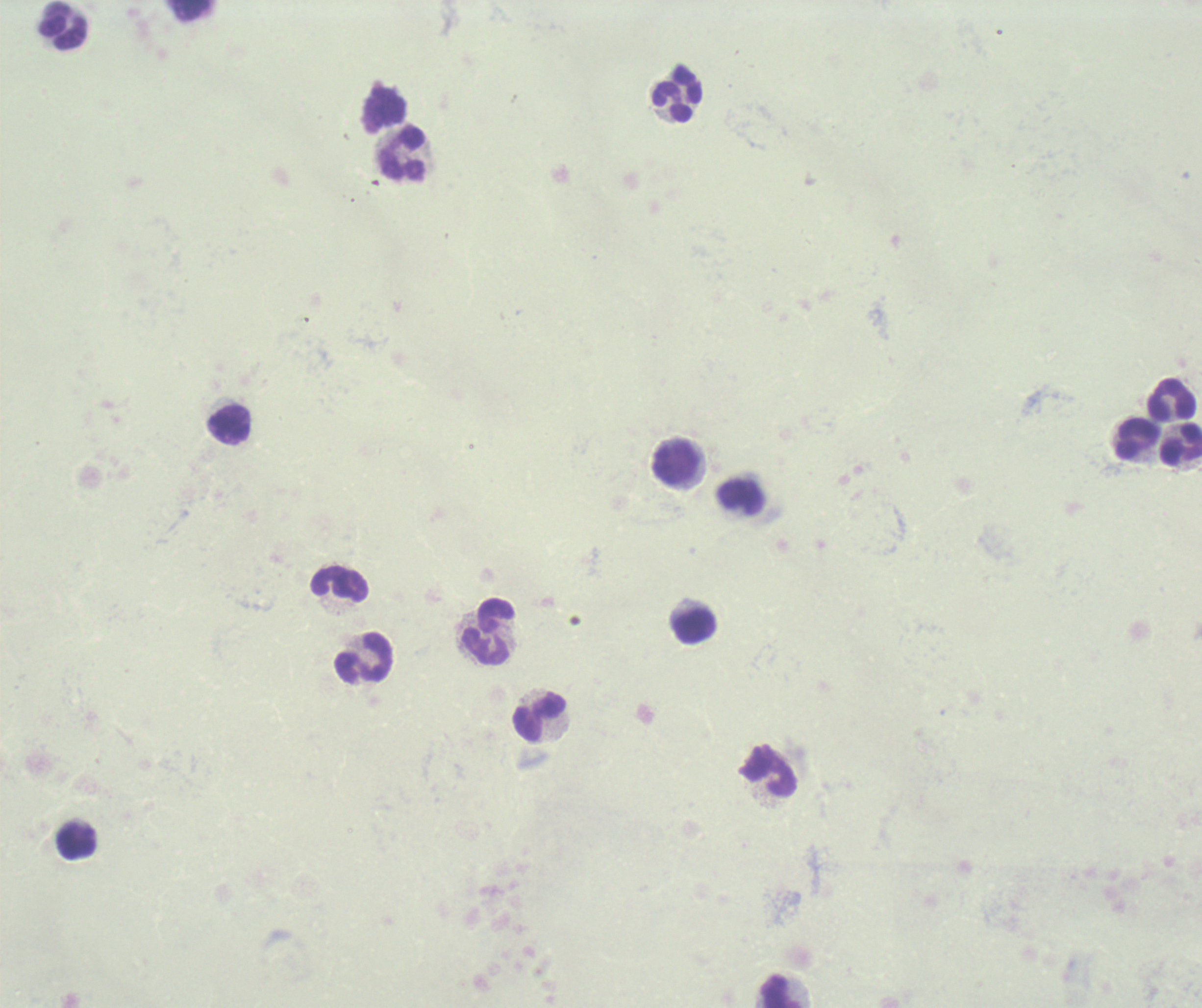
{
  "preparation": "thick blood film",
  "background_quality": "poor",
  "stain": "Romanowsky",
  "image_size": "1202×1008 pixels",
  "leukocyte_locations": "approximate object centers, in pixels from the top-left corner: (x=63, y=25), (x=678, y=95), (x=383, y=108), (x=402, y=155), (x=1171, y=400), (x=229, y=425), (x=1134, y=438), (x=1181, y=444), (x=677, y=465), (x=742, y=497), (x=339, y=586), (x=691, y=625), (x=489, y=633), (x=364, y=659), (x=539, y=718), (x=768, y=770), (x=76, y=840), (x=779, y=989)",
  "magnification": "100x",
  "context": "previously used in an actual diagnosis",
  "field_of_view": "one from this slide",
  "result": "no malaria parasites detected"
}